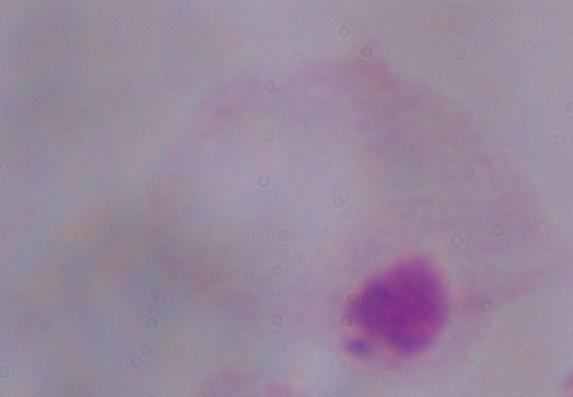 A trichomonad is shown. Captured at 1000x magnification. Photomicrograph.